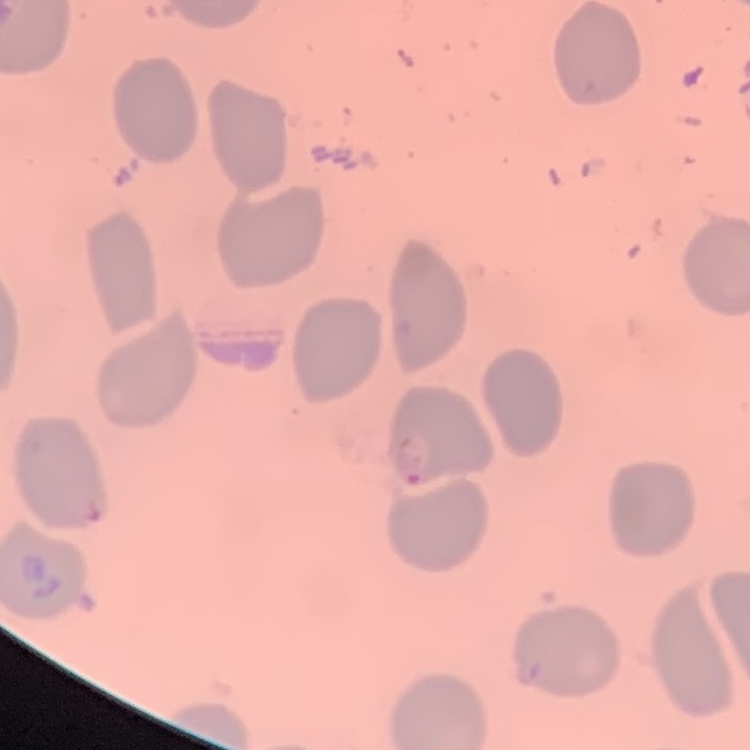
The red blood cells exhibit no rouleaux formation. Square crop of a larger photomicrograph. Stained with either Field's or Giemsa. Thin blood smear.